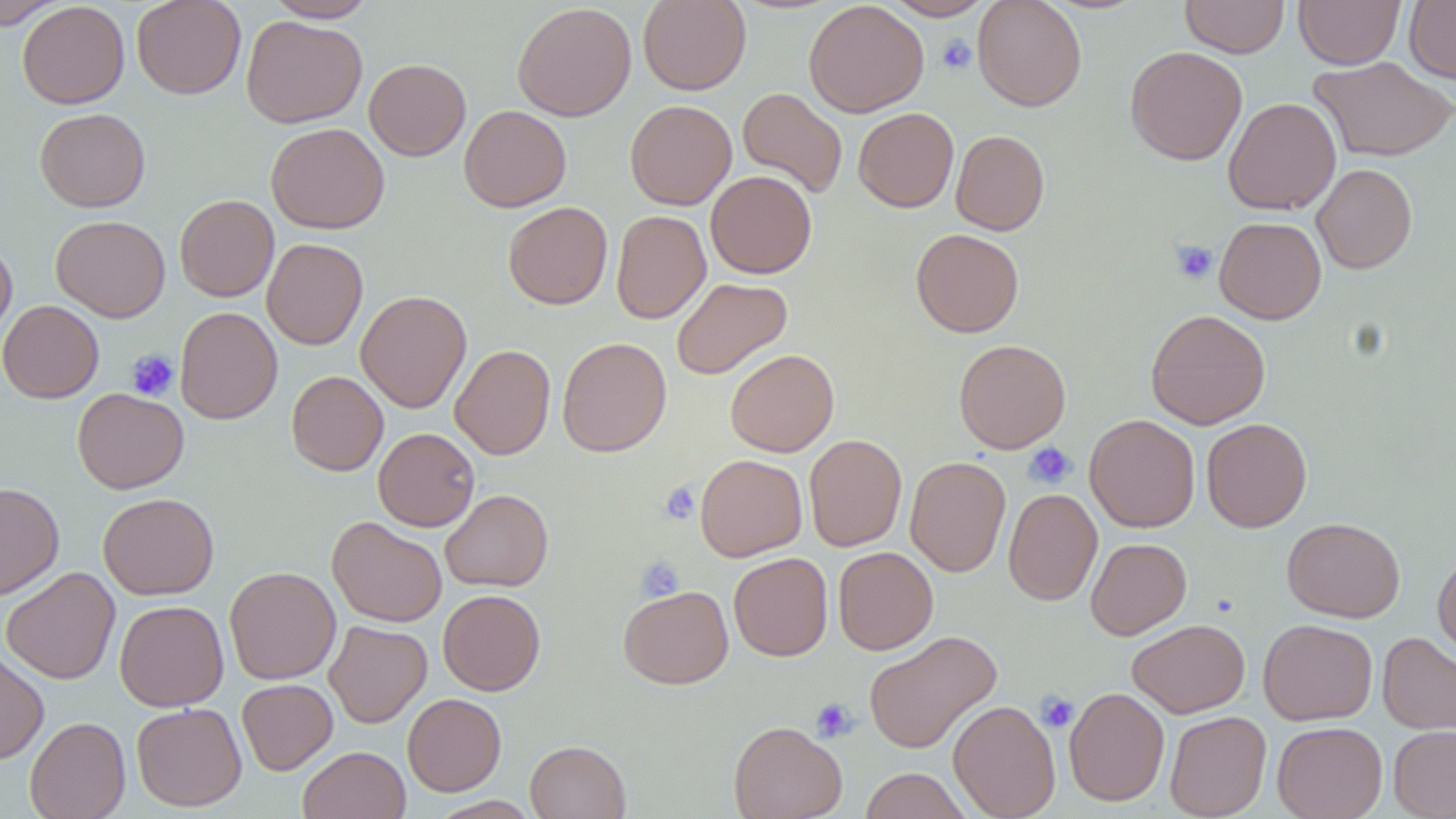
slide-level diagnosis = negative for blood parasites
stain = May-Grünwald-Giemsa
platelet locations = approximate bounding boxes as (x1,y1)-(x2,y2) corner pairs in pixels: (937,35)-(976,74), (1170,241)-(1218,284), (126,348)-(179,401), (1023,441)-(1077,489), (659,481)-(700,525), (636,555)-(684,601), (1036,692)-(1079,731), (810,697)-(858,742)
field of view = one of a larger specimen
preparation = thin blood film
magnification = 1000x
image size = 1456×819 pixels
uninfected red blood cell locations = approximate bounding boxes as (x1,y1)-(x2,y2) corner pairs in pixels: (0,0)-(66,28), (131,0)-(246,99), (266,0)-(377,22), (637,0)-(751,95), (803,0)-(929,117), (882,0)-(993,21), (972,0)-(1087,111), (1180,0)-(1289,58), (1294,0)-(1405,69), (1404,0)-(1456,84), (17,1)-(130,109), (512,2)-(637,122), (241,15)-(367,128), (1124,46)-(1247,165), (1309,56)-(1456,162), (364,58)-(471,160), (737,88)-(848,197), (1223,97)-(1341,215), (625,99)-(737,209), (459,105)-(571,212), (35,107)-(150,212), (854,107)-(958,212), (266,122)-(389,234), (950,129)-(1050,235), (1312,163)-(1417,273), (706,170)-(817,278), (175,194)-(279,302), (503,201)-(613,309), (611,210)-(711,324), (51,215)-(171,322), (1214,217)-(1326,324), (911,229)-(1024,337), (262,237)-(368,350), (0,240)-(17,343), (671,277)-(793,380), (356,289)-(472,413), (0,300)-(103,403), (174,306)-(282,424), (1145,309)-(1270,430), (557,337)-(671,457), (953,339)-(1070,453), (450,344)-(555,460), (725,349)-(839,457), (286,371)-(388,475), (72,388)-(189,493), (1084,414)-(1200,532), (1201,418)-(1312,532), (373,427)-(479,531), (804,434)-(907,551), (695,454)-(807,561), (905,456)-(1011,577), (0,482)-(64,600), (1003,487)-(1102,606), (440,489)-(553,592), (98,492)-(219,599), (327,517)-(447,627), (1282,517)-(1405,622), (1085,538)-(1191,639), (833,546)-(938,655), (1432,550)-(1456,662), (729,552)-(833,661), (224,566)-(341,684), (1,567)-(120,684), (618,584)-(734,689), (437,589)-(546,695), (114,599)-(228,711), (1127,618)-(1250,718), (1258,618)-(1378,725), (324,620)-(432,727), (863,630)-(1002,753), (1377,632)-(1456,736), (0,648)-(49,765), (237,678)-(338,774), (1064,687)-(1170,806), (403,693)-(506,796), (948,699)-(1061,819), (132,702)-(247,811), (1164,711)-(1271,819), (25,716)-(130,819), (728,720)-(847,819), (1272,721)-(1387,819), (1388,725)-(1456,819), (525,740)-(631,819), (298,745)-(410,819), (860,768)-(971,819), (428,796)-(542,818)
modality = light microscopy